Name the parasite shown.
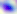

This is Toxoplasma gondii.

400x magnification. Photomicrograph.